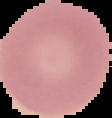

Summary:
  - Image type: segmented cell region on a black background
  - Image size: 112×118 pixels
  - Preparation: thin blood film
  - Result: negative for Plasmodium parasites